State which cell type is depicted.
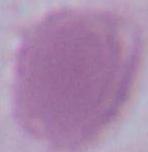
This is an erythrocyte.

Photomicrograph. 1000x magnification.